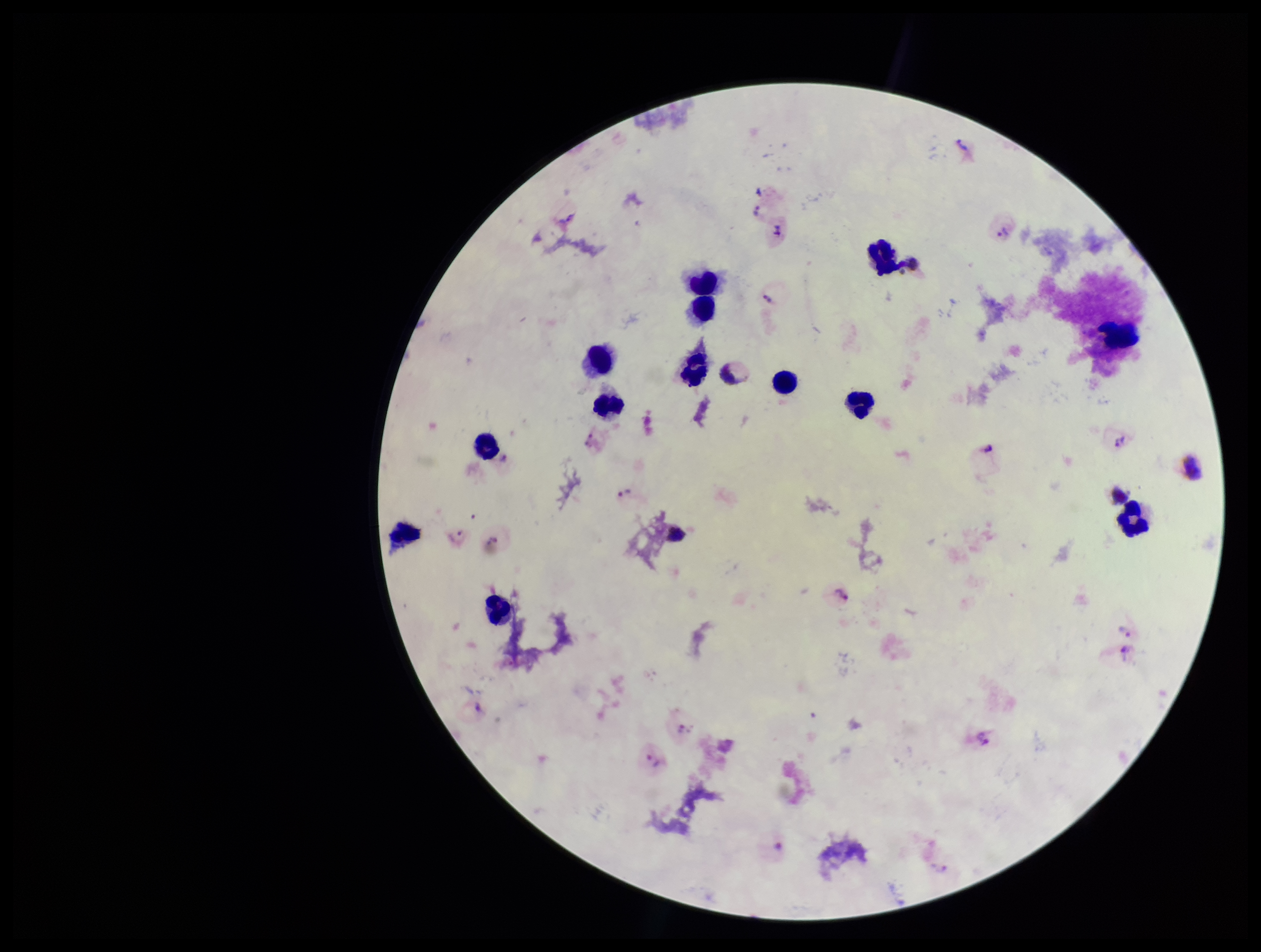

{
  "parasite_count": 8,
  "species_reported_for_this_patient": "Plasmodium vivax",
  "patient_malaria_status": "infected",
  "leukocyte_count": 13,
  "plasmodium_parasites": "detected",
  "capture": "smartphone photograph through the microscope eyepiece",
  "preparation": "thick blood smear",
  "stain": "Giemsa",
  "field_of_view": "single",
  "image_size": "1261×952 pixels"
}